Classify this cell by malaria status.
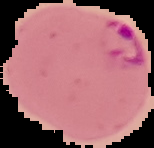

It is parasitized.

preparation: thin blood film
image_size: 154×148 pixels
image_type: cell region segmented out of the field of view; surrounding area masked to black